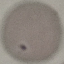
Summary:
  - Malaria status: uninfected
  - Preparation: thin blood film
  - Stain: Giemsa
  - Capture: smartphone through the microscope eyepiece
  - Image type: automatically extracted cell patch, resized to 64 × 64 pixels